Outline each blood parasite and name the species.
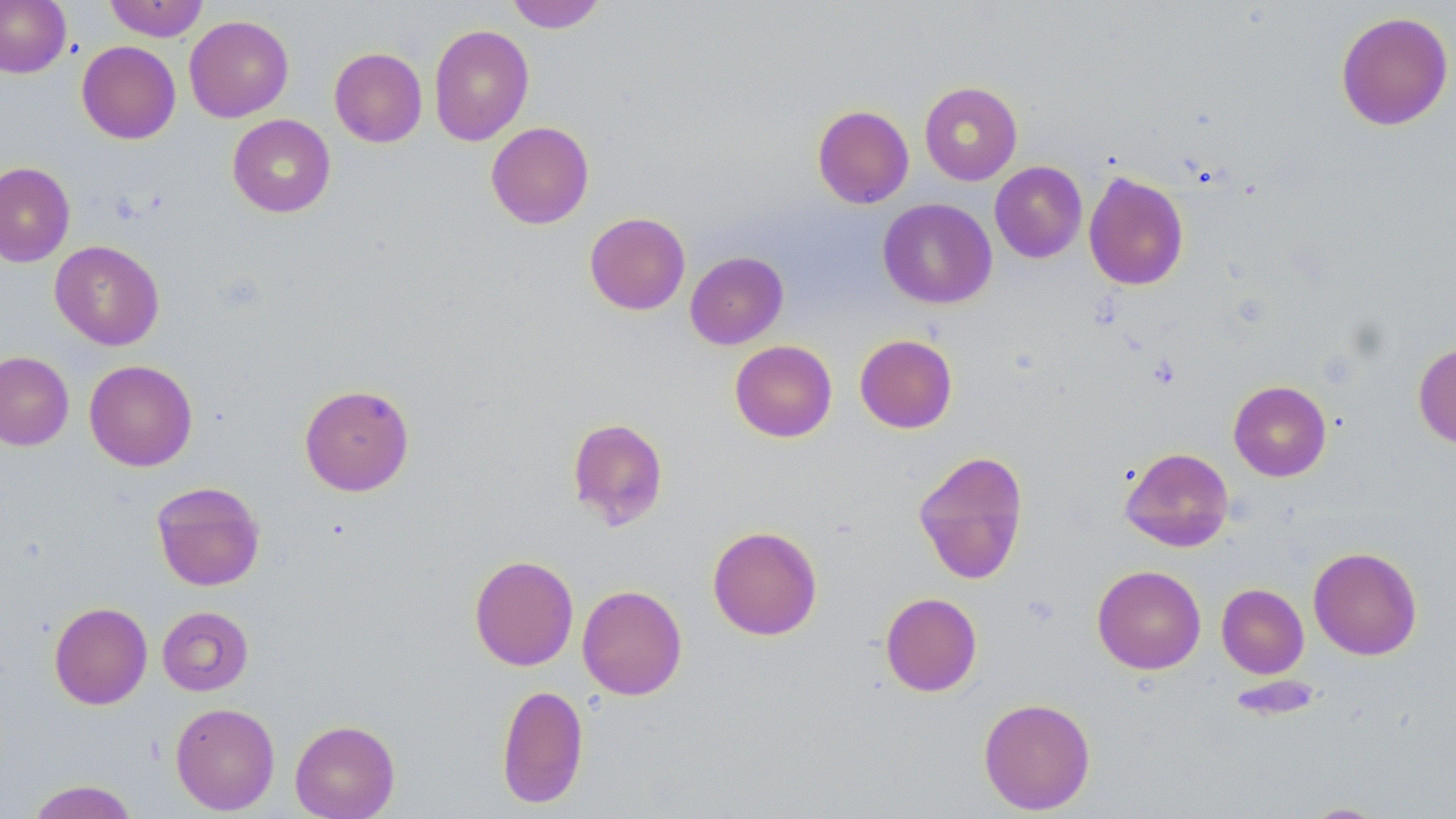

No blood parasites seen.

slide-level diagnosis = negative for blood parasites
magnification = 1000x
modality = optical microscopy
preparation = thin blood film
uninfected red blood cell locations = approximate bounding boxes as named x1/y1/x2/y2 corners in pixels: (x1=0, y1=0, x2=71, y2=77), (x1=103, y1=0, x2=209, y2=41), (x1=506, y1=0, x2=607, y2=33), (x1=1335, y1=11, x2=1454, y2=131), (x1=184, y1=15, x2=294, y2=122), (x1=428, y1=24, x2=534, y2=146), (x1=77, y1=41, x2=180, y2=144), (x1=329, y1=47, x2=427, y2=147), (x1=919, y1=81, x2=1023, y2=185), (x1=812, y1=104, x2=914, y2=209), (x1=227, y1=114, x2=336, y2=217), (x1=486, y1=121, x2=594, y2=229), (x1=990, y1=161, x2=1087, y2=263), (x1=0, y1=162, x2=75, y2=267), (x1=1083, y1=171, x2=1189, y2=290), (x1=879, y1=198, x2=997, y2=309), (x1=584, y1=212, x2=690, y2=315), (x1=50, y1=240, x2=164, y2=350), (x1=685, y1=251, x2=788, y2=350), (x1=855, y1=334, x2=958, y2=433), (x1=730, y1=340, x2=837, y2=442), (x1=1413, y1=341, x2=1456, y2=449), (x1=0, y1=351, x2=74, y2=451), (x1=84, y1=360, x2=197, y2=471), (x1=1228, y1=380, x2=1331, y2=481), (x1=299, y1=384, x2=415, y2=496), (x1=567, y1=417, x2=669, y2=530), (x1=1119, y1=446, x2=1234, y2=552), (x1=913, y1=449, x2=1029, y2=585), (x1=151, y1=481, x2=266, y2=591), (x1=707, y1=525, x2=823, y2=640), (x1=1308, y1=546, x2=1422, y2=660), (x1=469, y1=554, x2=579, y2=671), (x1=1092, y1=565, x2=1206, y2=674), (x1=1216, y1=583, x2=1309, y2=678), (x1=577, y1=584, x2=688, y2=700), (x1=880, y1=592, x2=982, y2=696), (x1=49, y1=602, x2=152, y2=710), (x1=157, y1=606, x2=253, y2=696), (x1=496, y1=684, x2=588, y2=808), (x1=978, y1=697, x2=1096, y2=814), (x1=170, y1=702, x2=280, y2=815), (x1=289, y1=719, x2=400, y2=819), (x1=26, y1=780, x2=139, y2=819), (x1=1298, y1=802, x2=1389, y2=818)
field of view = single
image size = 1456×819 pixels
stain = May-Grünwald-Giemsa